Name the parasite shown.
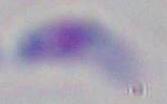
This is Toxoplasma gondii.

Micrograph. Captured at 1000x magnification.